Classify this cell by malaria status.
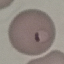
Parasitized.

image_type: cell patch, automatically extracted from a larger field of view and resized to 64 × 64 pixels
preparation: thin blood smear
capture: smartphone camera at the microscope eyepiece
stain: Giemsa